Identify the parasite.
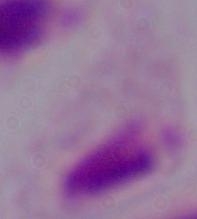

This is a trichomonad.

{
  "magnification": "1000x",
  "modality": "photomicrograph"
}